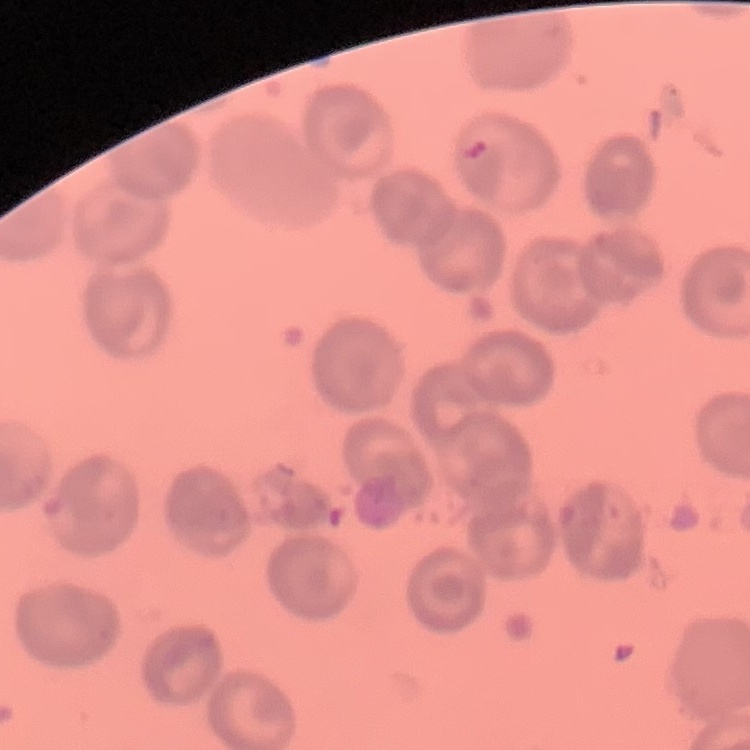
Summary:
  - Erythrocyte morphology: no rouleaux formation
  - Preparation: thin peripheral smear
  - Image type: square crop of a larger photomicrograph
  - Stain: Field's or Giemsa